Name the parasite shown.
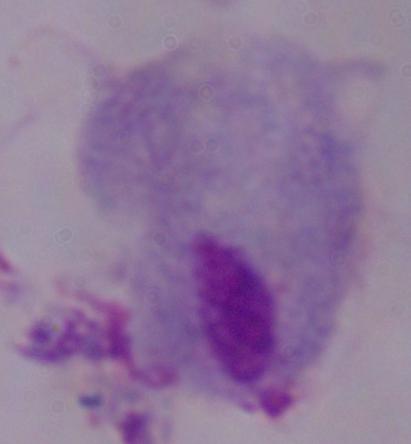
This is a trichomonad.

Captured at 1000x magnification. Photomicrograph.